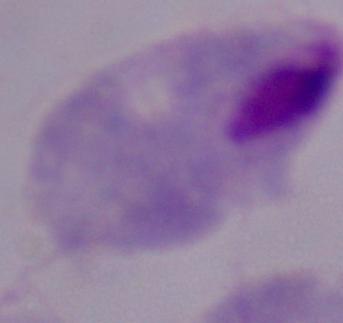 A trichomonad is shown. Micrograph. Captured at 1000x magnification.